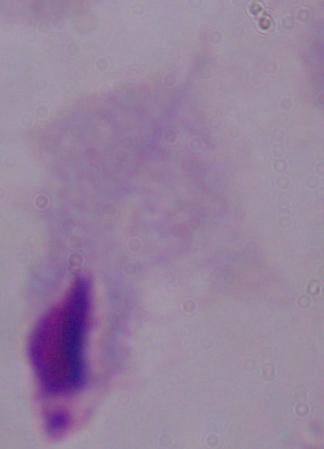

{
  "identification": "trichomonad",
  "modality": "photomicrograph",
  "magnification": "1000x"
}